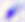

identification = Toxoplasma gondii
modality = micrograph
magnification = 400x